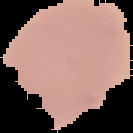

{
  "image_type": "segmented cell region on a black background",
  "preparation": "thin blood film",
  "malaria_status": "uninfected",
  "image_size": "133×133 pixels"
}